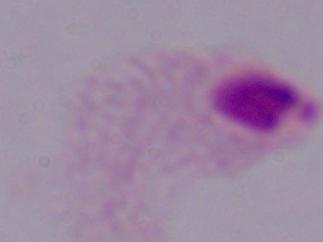
identification = trichomonad
magnification = 1000x
modality = photomicrograph